Report the malaria status of this cell.
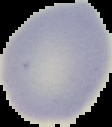
It is uninfected.

Summary:
  - Preparation: thin blood film
  - Image size: 112×127 pixels
  - Image type: segmented cell region on a black background